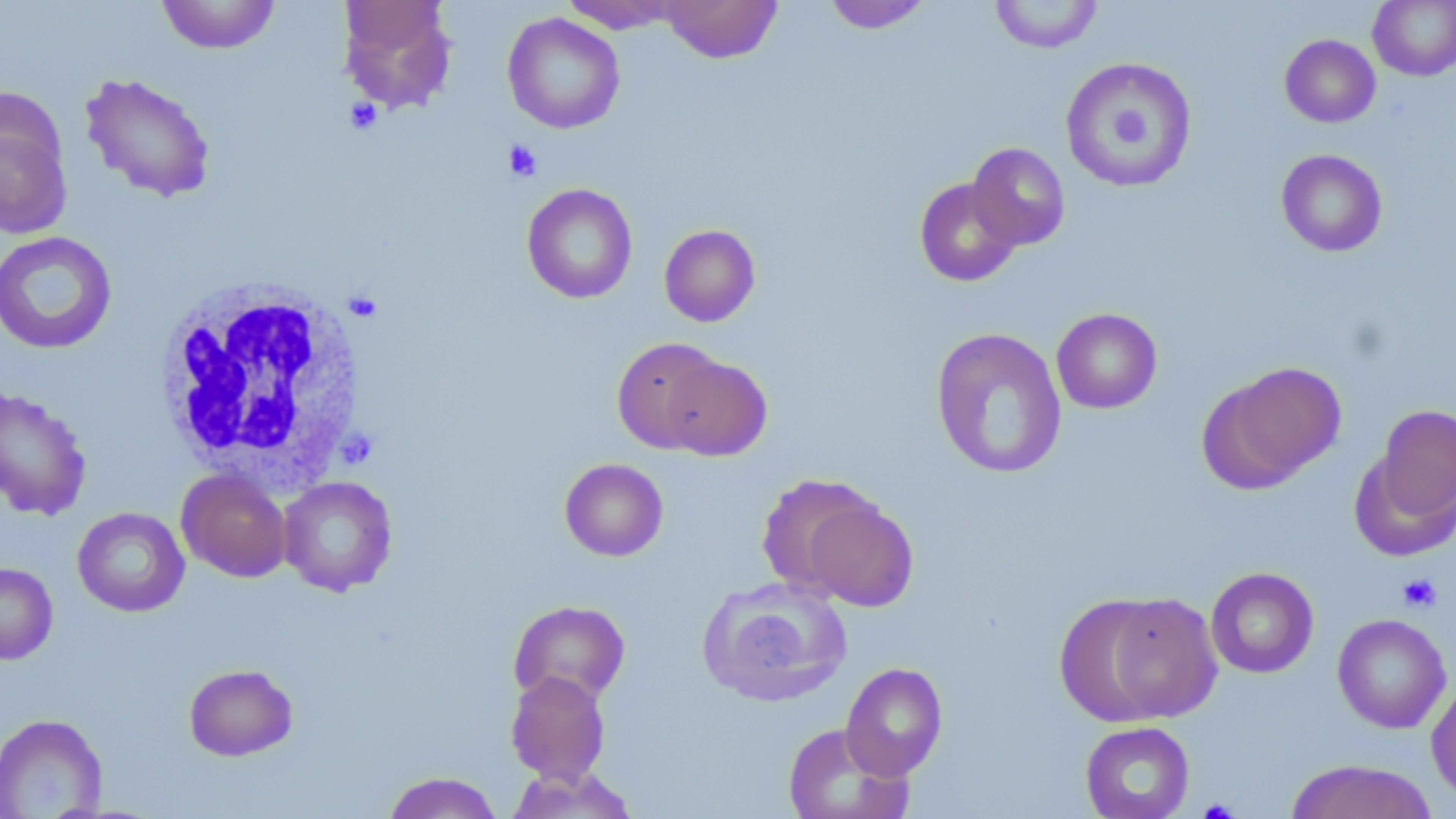

Approximate bounding boxes as (x1,y1)-(x2,y2) corner pairs in pixels. White blood cell locations: (152,279)-(370,487). Uninfected red blood cell locations: (156,0)-(280,54), (662,0)-(782,63), (822,0)-(932,34), (989,0)-(1104,54), (338,1)-(457,111), (561,1)-(682,34), (1367,1)-(1456,81), (502,13)-(625,134), (1279,34)-(1381,127), (1059,56)-(1198,192), (79,72)-(217,203), (0,99)-(73,241), (967,143)-(1071,251), (1275,149)-(1388,257), (914,177)-(1022,287), (521,183)-(638,304), (659,224)-(761,327), (0,231)-(118,355), (1052,308)-(1162,414), (930,327)-(1068,480), (611,337)-(728,453), (659,354)-(772,461), (1202,362)-(1346,490), (0,387)-(92,521), (1370,402)-(1456,527), (559,458)-(668,561), (177,468)-(291,582), (756,473)-(881,598), (278,476)-(398,596), (803,498)-(918,612), (72,507)-(190,617), (0,562)-(58,664), (1205,567)-(1319,679), (698,576)-(853,708), (1101,593)-(1222,723), (1054,596)-(1176,726), (508,600)-(631,707), (1332,613)-(1452,734), (841,662)-(948,780), (183,663)-(299,761), (505,671)-(611,785), (1427,677)-(1456,805), (0,713)-(108,818), (1080,721)-(1195,819), (782,723)-(912,819), (1284,759)-(1438,819), (505,765)-(638,818), (381,771)-(504,819). Platelet locations: (345,97)-(382,134), (503,140)-(542,182), (351,295)-(377,324), (1397,573)-(1442,613), (1198,799)-(1240,818). Slide-level diagnosis: no evidence of blood parasites. 1000x magnification. May-Grünwald-Giemsa stain. One field of a larger specimen. Image is 1456×819 pixels. Optical microscopy. Thin blood film.